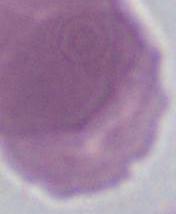

modality: photomicrograph
identification: erythrocyte
magnification: 1000x